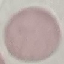
Summary:
  - Malaria status: uninfected
  - Preparation: thin smear
  - Stain: Giemsa
  - Capture: smartphone through the microscope eyepiece
  - Image type: automatically extracted cell patch, resized to 64 × 64 pixels